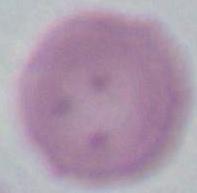
An erythrocyte is seen. Captured at 1000x magnification. Micrograph.